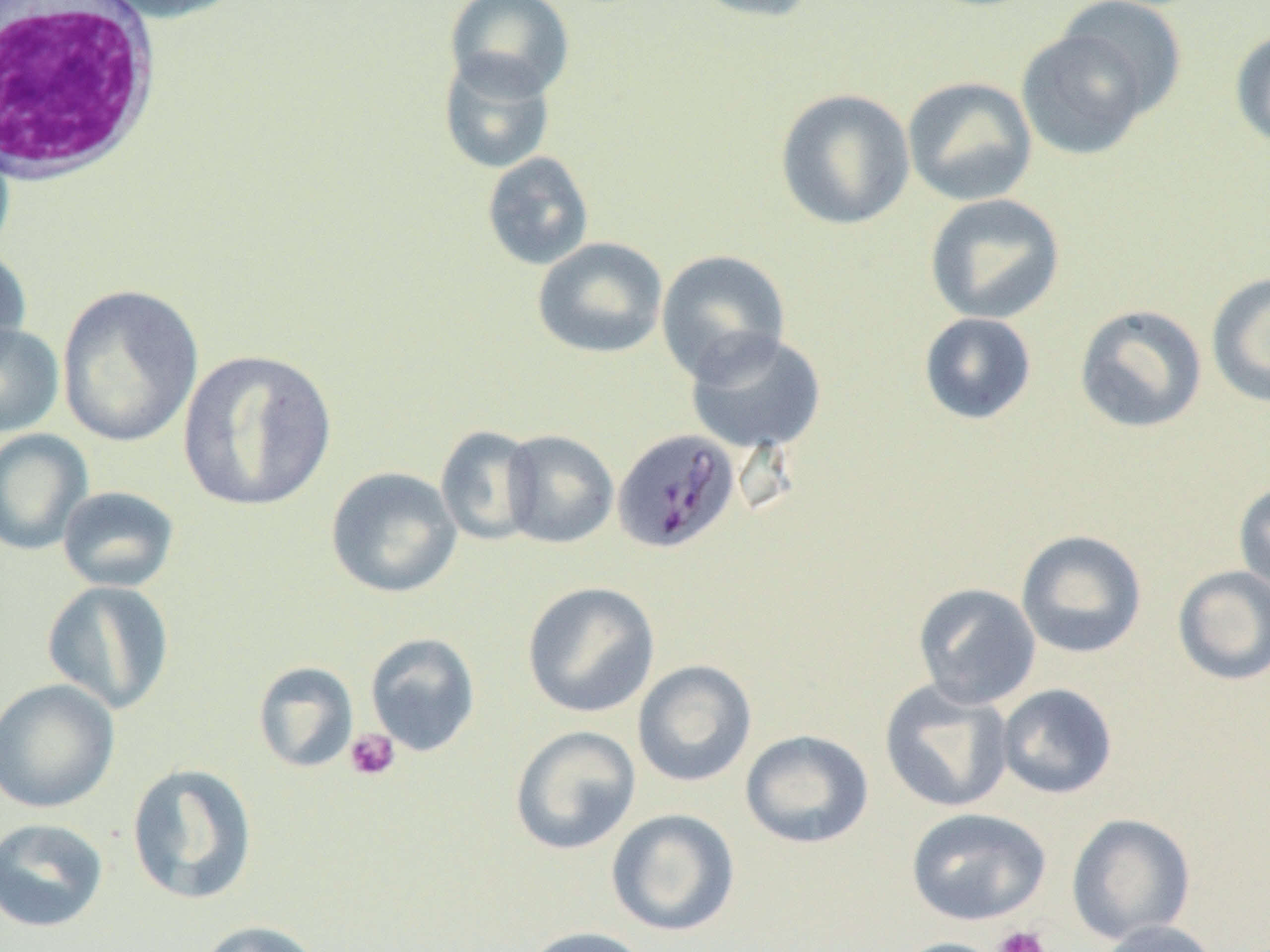

slide_level_diagnosis: Plasmodium malariae
white_blood_cell_locations: 'approximate bounding boxes as (x1,y1)-(x2,y2) corner pairs in pixels: (0,0)-(162,185)'
plasmodium_malariae_infected_red_blood_cell_locations: 'approximate bounding boxes as (x1,y1)-(x2,y2) corner pairs in pixels: (614,427)-(743,555)'
preparation: thin blood smear
image_size: 1270×952 pixels
uninfected_red_blood_cell_locations: 'approximate bounding boxes as (x1,y1)-(x2,y2) corner pairs in pixels: (93,0)-(248,23), (445,0)-(575,100), (685,0)-(822,23), (1052,0)-(1189,121), (1016,27)-(1156,161), (1230,28)-(1270,151), (438,52)-(556,174), (902,76)-(1038,206), (774,88)-(915,230), (481,152)-(595,271), (924,193)-(1065,325), (532,237)-(668,358), (0,245)-(31,367), (656,249)-(791,383), (1206,272)-(1270,409), (57,284)-(205,448), (1074,304)-(1207,434), (918,312)-(1037,425), (0,322)-(64,436), (685,328)-(826,454), (177,348)-(338,513), (435,425)-(541,546), (0,429)-(94,556), (501,430)-(618,548), (325,467)-(462,599), (1233,480)-(1270,597), (57,486)-(179,593), (1016,529)-(1147,659), (1172,565)-(1270,686), (41,579)-(175,715), (522,581)-(659,718), (912,582)-(1042,709), (365,632)-(481,757), (632,660)-(757,787), (253,661)-(359,773), (0,677)-(120,814), (879,679)-(1015,813), (996,683)-(1117,799), (509,725)-(642,855), (740,729)-(874,849), (126,762)-(258,905), (606,808)-(741,937), (906,808)-(1051,926), (1066,812)-(1197,944), (0,817)-(109,933), (195,919)-(325,952), (1094,920)-(1222,952), (521,926)-(655,952), (889,937)-(1012,952)'
field_of_view: one of a larger specimen
platelet_locations: 'approximate bounding boxes as (x1,y1)-(x2,y2) corner pairs in pixels: (344,728)-(400,781), (992,925)-(1050,952)'
magnification: 1000x
modality: optical microscopy